Locate every blood parasite and identify its species.
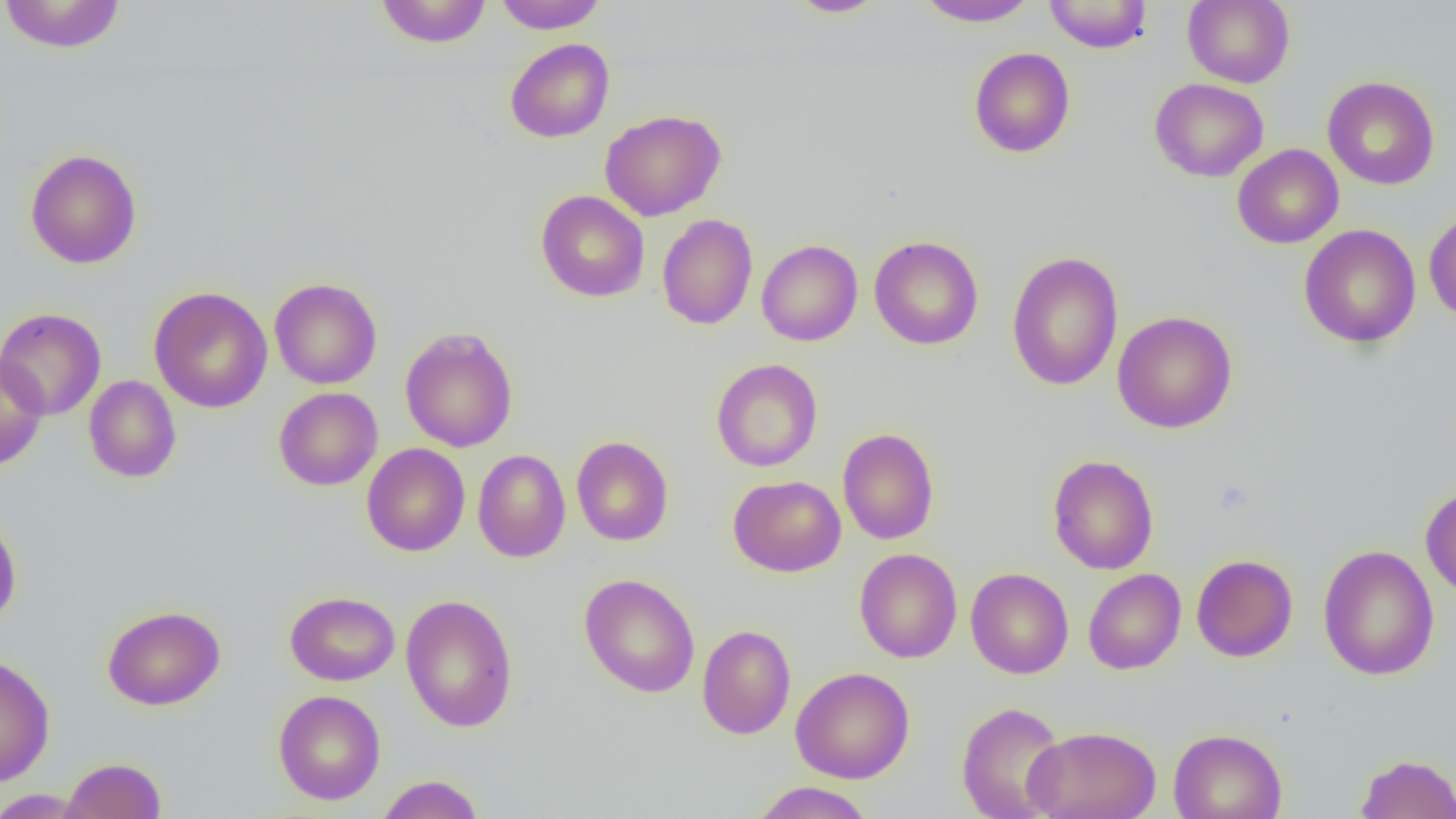
No blood parasites observed.

slide-level diagnosis = negative for blood parasites
field of view = single
image size = 1456×819 pixels
magnification = 1000x
modality = light microscopy
uninfected red blood cell locations = approximate bounding boxes as (x1, y1, x2, y2) in pixels: (0, 0, 127, 54), (375, 0, 491, 48), (493, 0, 608, 33), (1043, 0, 1153, 53), (1183, 0, 1295, 88), (784, 1, 889, 18), (914, 1, 1040, 27), (505, 38, 615, 143), (968, 47, 1076, 158), (1322, 76, 1439, 190), (1150, 77, 1269, 182), (600, 109, 726, 221), (1232, 144, 1344, 249), (25, 148, 142, 269), (536, 190, 650, 302), (1424, 208, 1456, 323), (657, 213, 758, 330), (1298, 224, 1421, 348), (869, 235, 983, 350), (756, 239, 863, 346), (1006, 250, 1123, 391), (269, 278, 382, 389), (149, 286, 273, 413), (0, 307, 106, 420), (1112, 310, 1238, 434), (400, 327, 518, 453), (0, 352, 49, 471), (711, 358, 823, 472), (83, 375, 181, 483), (273, 387, 383, 491), (838, 428, 939, 545), (571, 436, 674, 546), (362, 444, 470, 556), (472, 449, 570, 562), (1047, 454, 1159, 574), (728, 475, 846, 576), (1420, 485, 1456, 598), (0, 514, 22, 628), (1317, 545, 1439, 681), (854, 548, 962, 663), (1191, 554, 1298, 662), (965, 567, 1074, 679), (1083, 568, 1186, 674), (578, 573, 701, 698), (285, 591, 399, 686), (400, 594, 518, 733), (102, 605, 225, 711), (697, 624, 796, 740), (0, 653, 55, 788), (791, 666, 914, 784), (273, 690, 386, 805), (956, 701, 1068, 819), (1024, 725, 1162, 819), (1168, 728, 1287, 819), (1355, 753, 1456, 818), (60, 757, 167, 819), (375, 775, 485, 819), (750, 781, 876, 819), (0, 789, 88, 818)
preparation = thin blood film